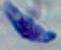
modality = micrograph
identification = Toxoplasma gondii
magnification = 1000x